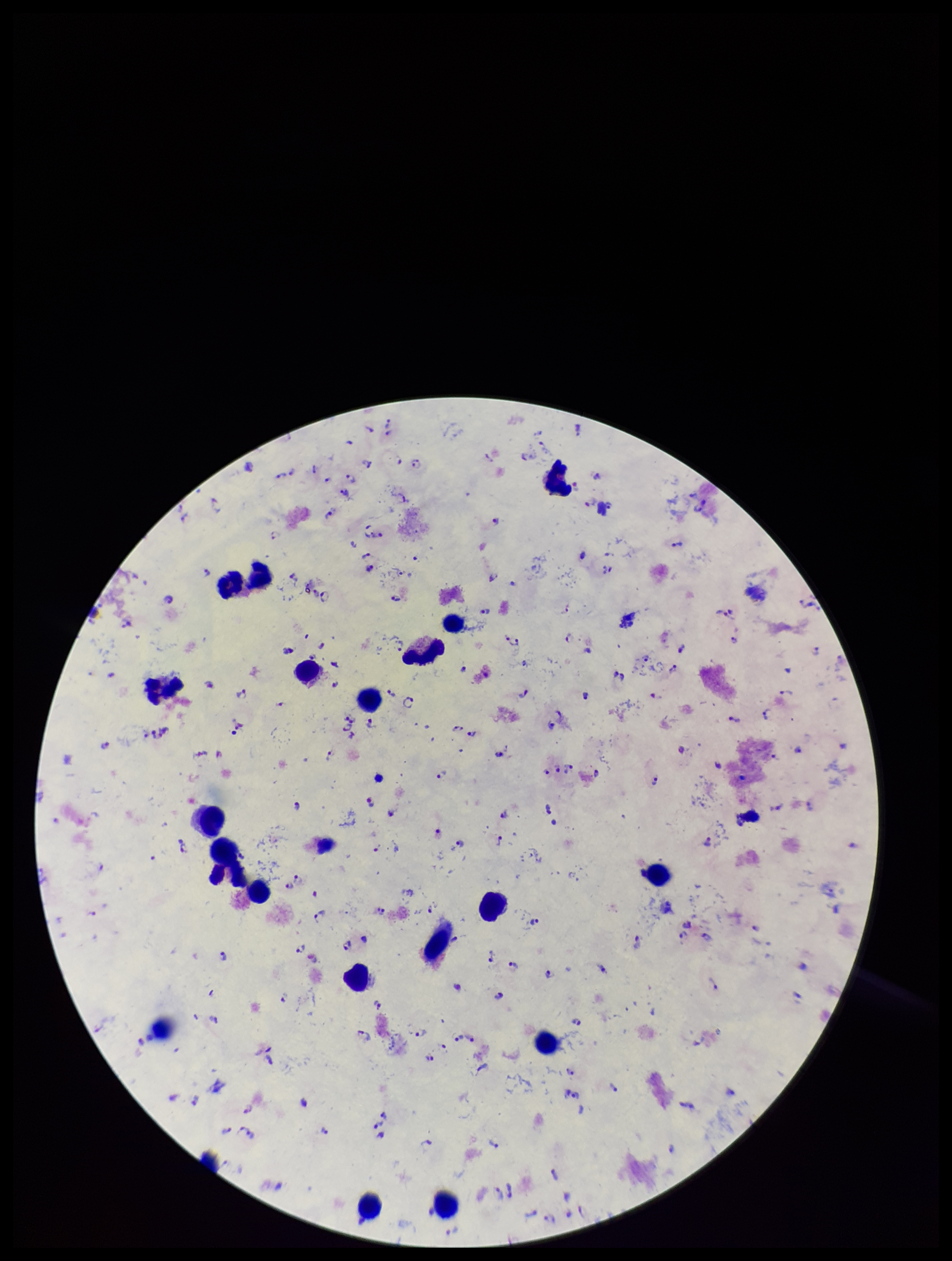

Summary:
  - Preparation: thick smear
  - Patient malaria status: infected
  - Plasmodium parasites: seen
  - Image size: 952×1261 pixels
  - Capture: smartphone photograph through the microscope eyepiece
  - Species reported for this patient: Plasmodium falciparum
  - Leukocyte count: 21
  - Stain: Giemsa
  - Field of view: one from this slide
  - Parasite count: 124